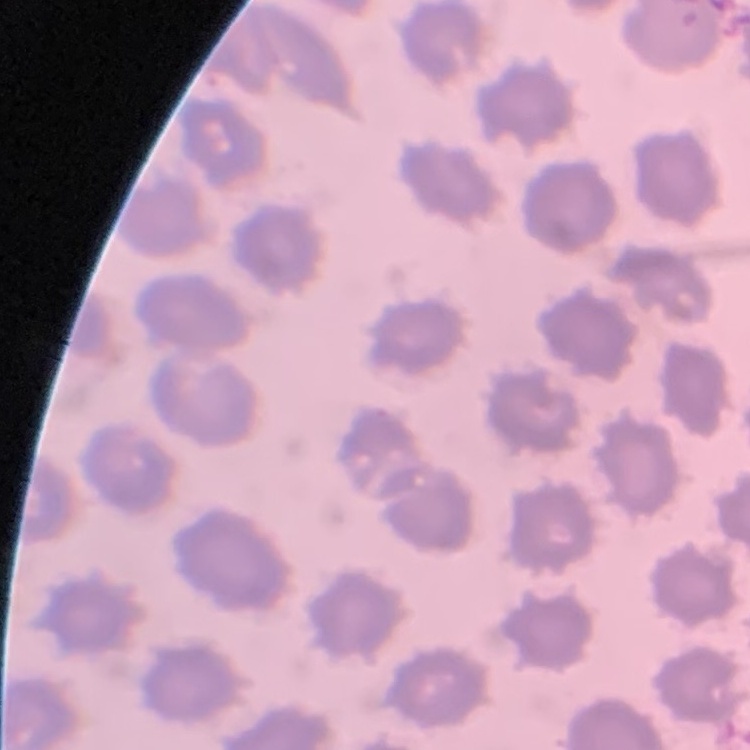
red blood cell morphology = no rouleaux formation
preparation = thin blood film
stain = Field's or Giemsa
image type = square crop of a larger photomicrograph